Classify this cell by malaria status.
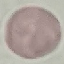
Uninfected.

Cell patch, automatically extracted from a larger field of view and resized to 64 × 64 pixels. Giemsa-stained preparation. Thin smear of blood. Photographed with a smartphone camera at the microscope eyepiece.